Classify this cell by malaria status.
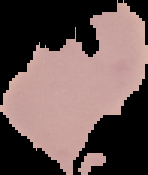
It is uninfected.

Summary:
  - Image size: 148×175 pixels
  - Image type: cell region segmented out of the field of view; surrounding area masked to black
  - Preparation: thin blood film